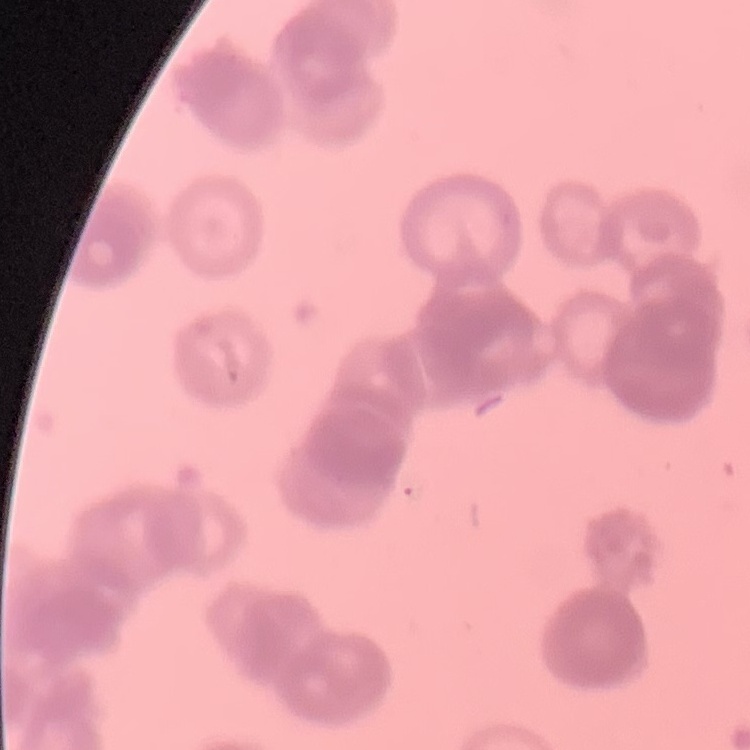

{
  "erythrocyte_morphology": "rouleaux formation",
  "stain": "Field's or Giemsa",
  "preparation": "thin blood smear",
  "image_type": "square crop of a larger photomicrograph"
}